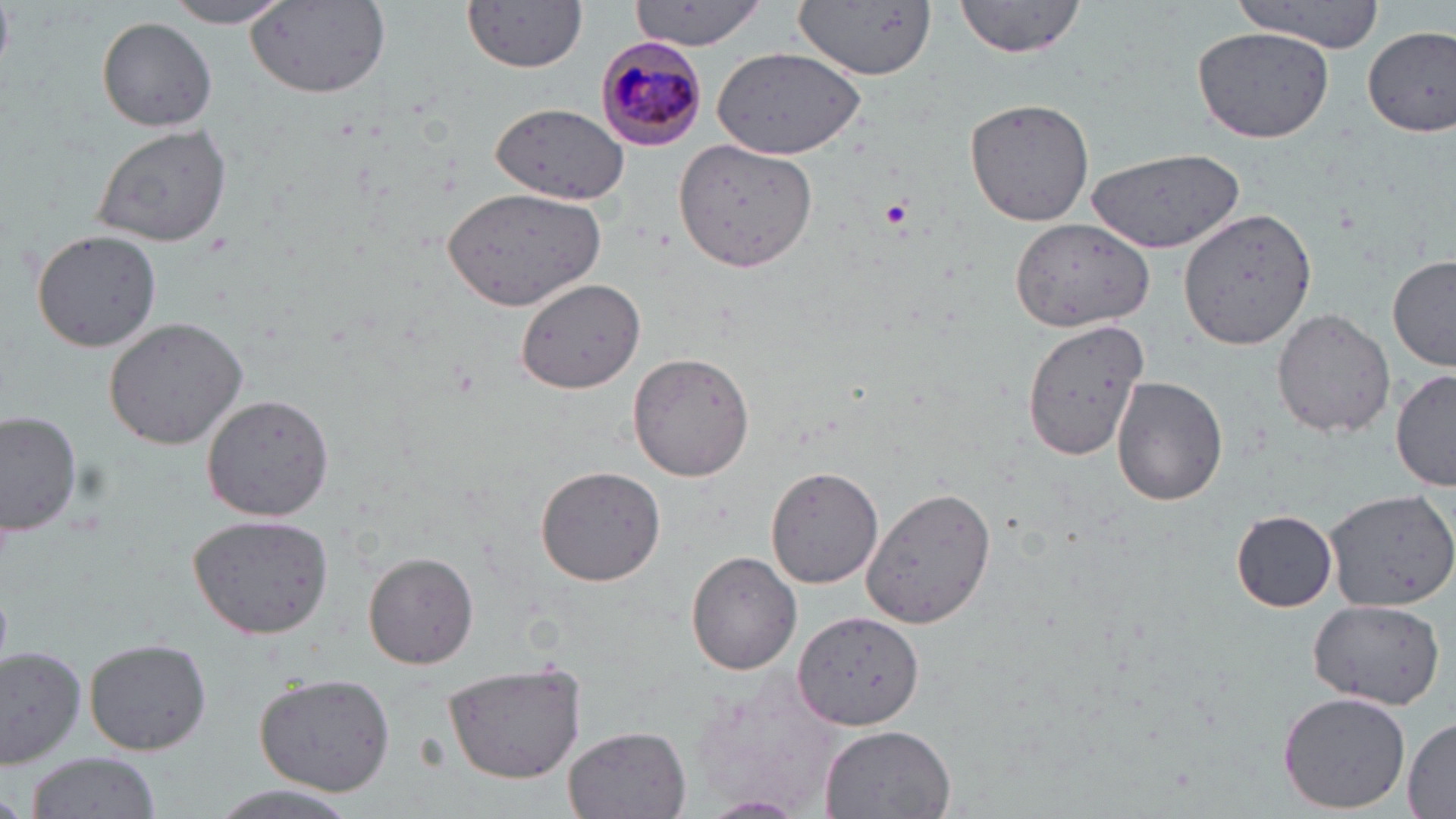
slide-level diagnosis = Plasmodium malariae
preparation = thin blood smear
Plasmodium malariae-infected red blood cell locations = approximate bounding boxes as named x1/y1/x2/y2 corners in pixels: (x1=597, y1=39, x2=709, y2=149)
uninfected red blood cell locations = approximate bounding boxes as named x1/y1/x2/y2 corners in pixels: (x1=172, y1=0, x2=287, y2=28), (x1=244, y1=0, x2=392, y2=100), (x1=464, y1=0, x2=587, y2=73), (x1=631, y1=0, x2=771, y2=51), (x1=792, y1=0, x2=937, y2=82), (x1=952, y1=0, x2=1089, y2=59), (x1=1230, y1=0, x2=1388, y2=50), (x1=95, y1=15, x2=219, y2=131), (x1=1192, y1=25, x2=1333, y2=142), (x1=1364, y1=27, x2=1456, y2=137), (x1=712, y1=48, x2=864, y2=161), (x1=964, y1=98, x2=1095, y2=227), (x1=490, y1=103, x2=629, y2=203), (x1=91, y1=123, x2=232, y2=247), (x1=675, y1=137, x2=818, y2=271), (x1=1086, y1=146, x2=1245, y2=254), (x1=442, y1=189, x2=608, y2=309), (x1=1180, y1=207, x2=1317, y2=348), (x1=1009, y1=218, x2=1154, y2=332), (x1=31, y1=229, x2=162, y2=352), (x1=1388, y1=254, x2=1456, y2=370), (x1=514, y1=277, x2=646, y2=394), (x1=1272, y1=309, x2=1395, y2=437), (x1=102, y1=316, x2=249, y2=450), (x1=1016, y1=316, x2=1150, y2=461), (x1=628, y1=352, x2=757, y2=482), (x1=1391, y1=370, x2=1456, y2=490), (x1=1110, y1=376, x2=1228, y2=506), (x1=201, y1=395, x2=334, y2=521), (x1=0, y1=411, x2=81, y2=537), (x1=535, y1=465, x2=665, y2=587), (x1=767, y1=468, x2=882, y2=589), (x1=862, y1=487, x2=997, y2=627), (x1=1323, y1=487, x2=1456, y2=610), (x1=1230, y1=510, x2=1339, y2=612), (x1=188, y1=514, x2=335, y2=641), (x1=363, y1=551, x2=479, y2=669), (x1=686, y1=551, x2=803, y2=675), (x1=1306, y1=597, x2=1446, y2=710), (x1=796, y1=612, x2=926, y2=730), (x1=82, y1=639, x2=211, y2=756), (x1=0, y1=647, x2=86, y2=769), (x1=442, y1=663, x2=589, y2=783), (x1=689, y1=670, x2=852, y2=817), (x1=252, y1=673, x2=396, y2=795), (x1=1276, y1=690, x2=1412, y2=814), (x1=1404, y1=715, x2=1455, y2=816), (x1=817, y1=724, x2=956, y2=818), (x1=562, y1=725, x2=691, y2=819), (x1=21, y1=751, x2=161, y2=819), (x1=704, y1=795, x2=808, y2=815)
modality = optical microscopy
platelet locations = approximate bounding boxes as named x1/y1/x2/y2 corners in pixels: (x1=878, y1=195, x2=914, y2=234)
magnification = 1000x
stain = May-Grünwald-Giemsa
field of view = one of a larger specimen
image size = 1456×819 pixels